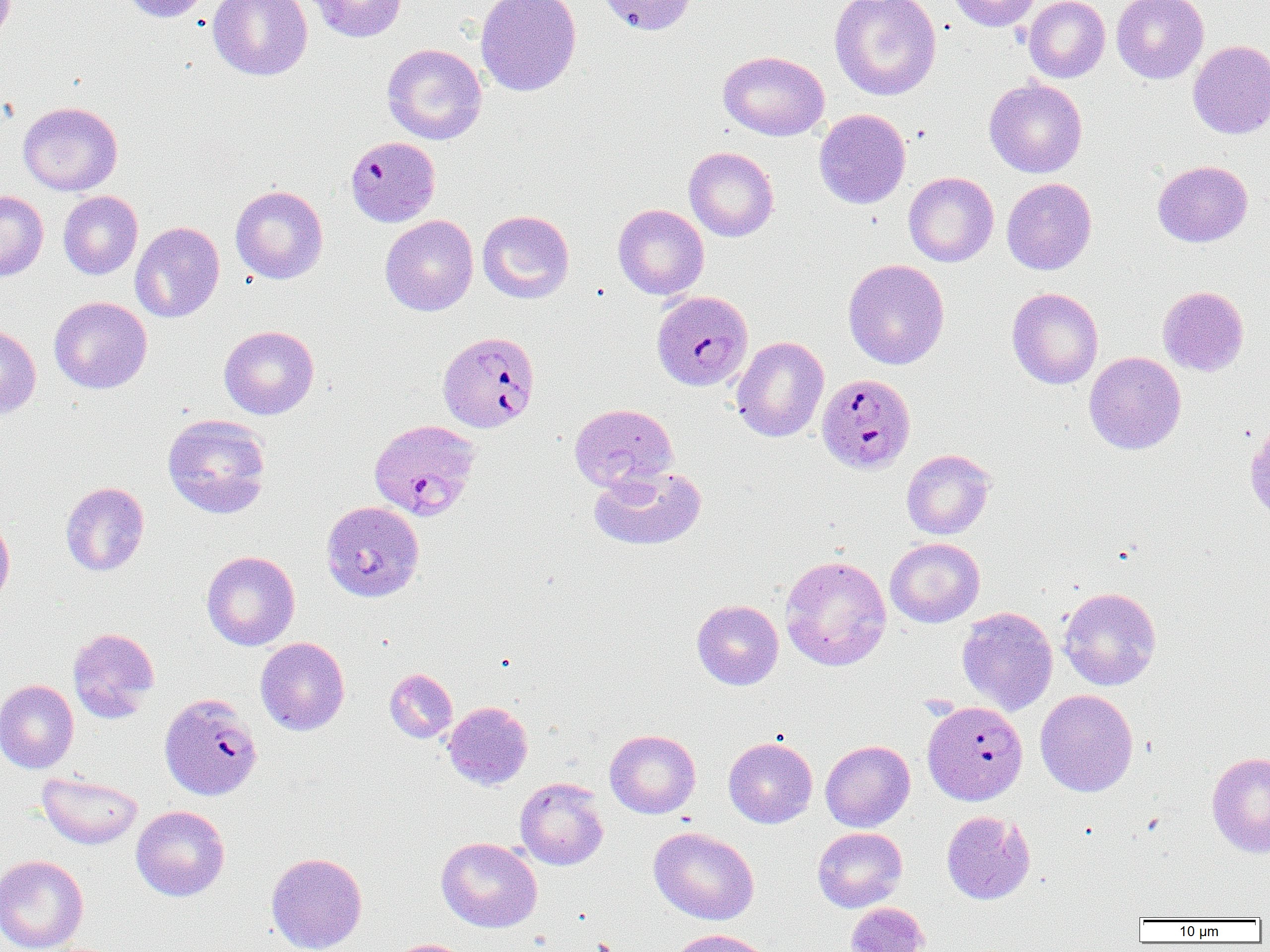

Summary:
  - Coordinate format: approximate bounding boxes as named x1/y1/x2/y2 corners in pixels
  - Uninfected red blood cell locations: (x1=119, y1=0, x2=211, y2=22), (x1=208, y1=0, x2=312, y2=81), (x1=307, y1=0, x2=408, y2=42), (x1=475, y1=0, x2=581, y2=97), (x1=595, y1=0, x2=696, y2=36), (x1=829, y1=0, x2=942, y2=101), (x1=945, y1=0, x2=1041, y2=31), (x1=1023, y1=0, x2=1110, y2=83), (x1=1111, y1=0, x2=1208, y2=84), (x1=1188, y1=40, x2=1270, y2=139), (x1=382, y1=44, x2=487, y2=145), (x1=719, y1=50, x2=829, y2=141), (x1=984, y1=78, x2=1087, y2=178), (x1=18, y1=101, x2=123, y2=195), (x1=814, y1=109, x2=911, y2=209), (x1=684, y1=147, x2=779, y2=242), (x1=1152, y1=160, x2=1253, y2=247), (x1=903, y1=172, x2=999, y2=267), (x1=1001, y1=177, x2=1097, y2=275), (x1=230, y1=185, x2=328, y2=284), (x1=0, y1=190, x2=48, y2=282), (x1=58, y1=191, x2=143, y2=279), (x1=613, y1=204, x2=709, y2=299), (x1=477, y1=210, x2=575, y2=304), (x1=380, y1=214, x2=478, y2=316), (x1=130, y1=221, x2=224, y2=323), (x1=843, y1=258, x2=949, y2=370), (x1=1157, y1=286, x2=1249, y2=376), (x1=1006, y1=287, x2=1103, y2=389), (x1=49, y1=296, x2=152, y2=394), (x1=0, y1=323, x2=41, y2=419), (x1=219, y1=325, x2=319, y2=420), (x1=731, y1=336, x2=829, y2=442), (x1=1084, y1=351, x2=1186, y2=455), (x1=569, y1=403, x2=678, y2=491), (x1=162, y1=413, x2=271, y2=519), (x1=1244, y1=423, x2=1270, y2=523), (x1=901, y1=449, x2=994, y2=540), (x1=588, y1=465, x2=707, y2=551), (x1=60, y1=482, x2=150, y2=576), (x1=321, y1=501, x2=424, y2=601), (x1=0, y1=513, x2=15, y2=608), (x1=885, y1=537, x2=984, y2=628), (x1=201, y1=551, x2=300, y2=650), (x1=780, y1=554, x2=892, y2=671), (x1=1058, y1=586, x2=1161, y2=690), (x1=692, y1=599, x2=784, y2=690), (x1=958, y1=602, x2=1160, y2=703), (x1=957, y1=606, x2=1058, y2=715), (x1=67, y1=627, x2=160, y2=723), (x1=255, y1=637, x2=350, y2=735), (x1=384, y1=668, x2=458, y2=743), (x1=0, y1=679, x2=79, y2=774), (x1=1035, y1=689, x2=1138, y2=797), (x1=442, y1=701, x2=533, y2=790), (x1=604, y1=729, x2=701, y2=818), (x1=724, y1=737, x2=817, y2=828), (x1=820, y1=740, x2=915, y2=832), (x1=1207, y1=751, x2=1270, y2=858), (x1=37, y1=771, x2=143, y2=849), (x1=515, y1=777, x2=609, y2=870), (x1=131, y1=805, x2=230, y2=901), (x1=941, y1=810, x2=1035, y2=905), (x1=648, y1=826, x2=759, y2=925), (x1=812, y1=827, x2=907, y2=912), (x1=436, y1=837, x2=542, y2=932), (x1=266, y1=852, x2=367, y2=952), (x1=0, y1=854, x2=89, y2=952), (x1=846, y1=902, x2=929, y2=952), (x1=667, y1=928, x2=775, y2=952), (x1=385, y1=939, x2=472, y2=952)
  - Plasmodium falciparum-infected red blood cell locations: (x1=343, y1=137, x2=441, y2=228), (x1=651, y1=290, x2=753, y2=391), (x1=437, y1=331, x2=540, y2=433), (x1=815, y1=373, x2=916, y2=473), (x1=369, y1=418, x2=481, y2=521), (x1=159, y1=694, x2=262, y2=800), (x1=922, y1=700, x2=1028, y2=805)
  - Slide-level diagnosis: Plasmodium falciparum
  - Image size: 1270×952 pixels
  - Field of view: one of a larger specimen
  - Magnification: 1000x
  - Modality: optical microscopy
  - Preparation: thin blood film